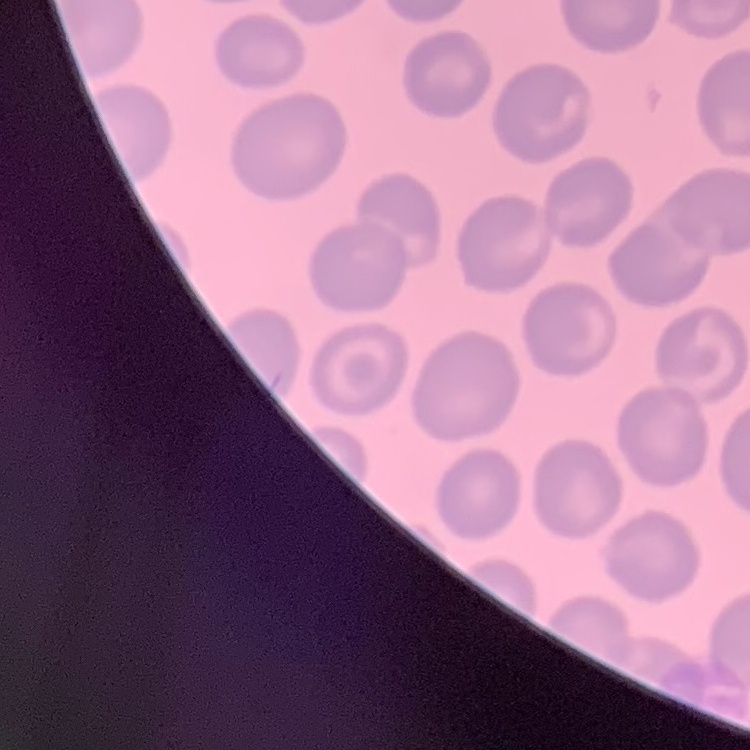

Summary:
  - Erythrocyte morphology: no rouleaux formation
  - Preparation: thin blood film
  - Image type: one tile cut from a larger photomicrograph
  - Stain: Field's or Giemsa